Locate every blood parasite and identify its species.
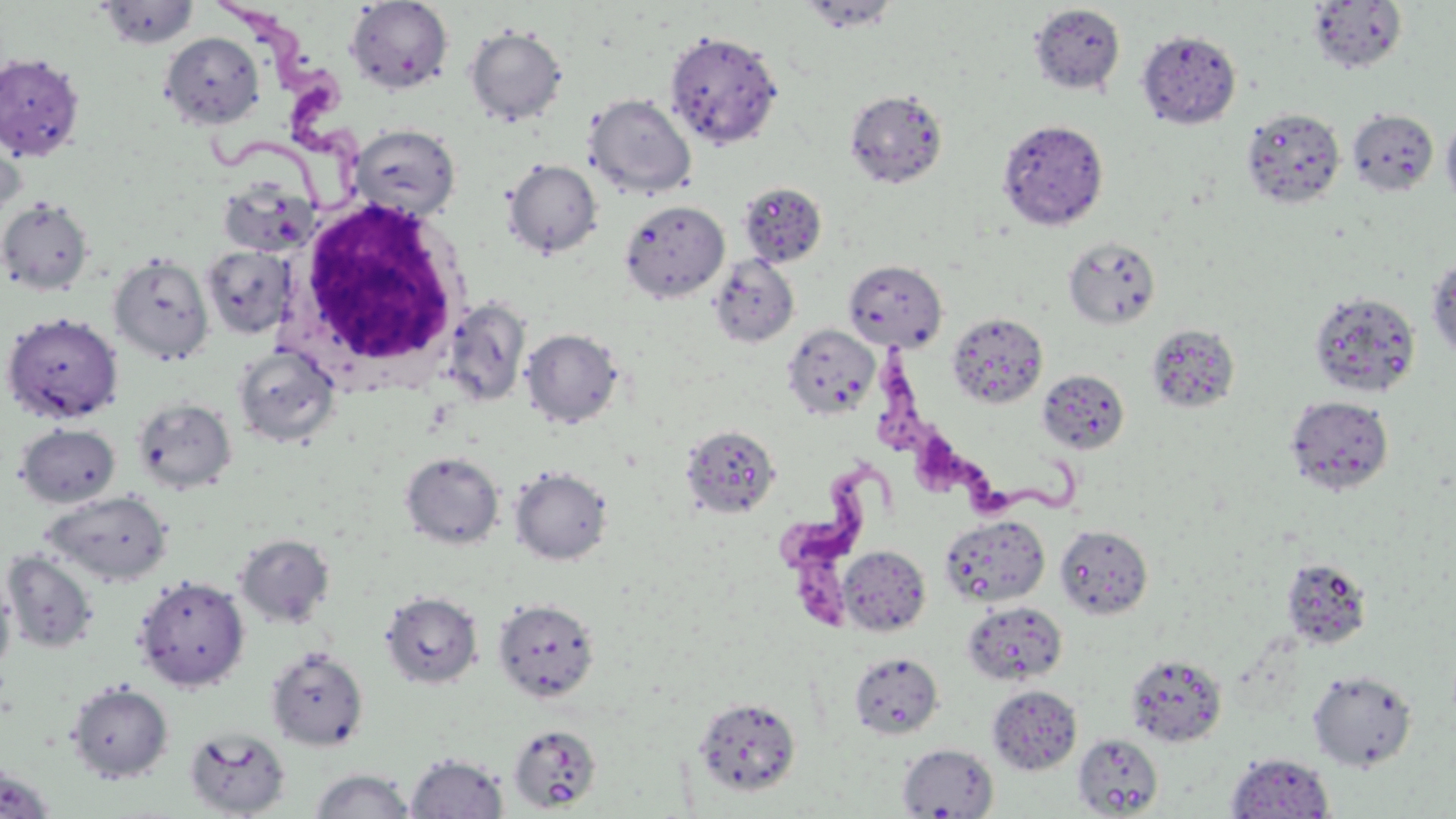
Approximate bounding boxes as (x1, y1, x2, y2) in pixels.
Trypanosoma brucei: (206, 0, 371, 211), (871, 340, 1087, 525), (775, 456, 898, 632).
No Plasmodium falciparum, Plasmodium ovale, Plasmodium malariae, Plasmodium vivax, or Babesia divergens observed.

White blood cell locations: (296, 196, 470, 373). Uninfected red blood cell locations: (797, 0, 901, 33), (96, 1, 200, 49), (345, 1, 454, 94), (1307, 1, 1407, 74), (1029, 3, 1126, 95), (464, 25, 568, 126), (1137, 29, 1241, 129), (664, 30, 783, 148), (160, 32, 264, 128), (0, 52, 86, 161), (844, 89, 949, 188), (585, 94, 697, 198), (1241, 107, 1346, 209), (1348, 109, 1439, 196), (1441, 114, 1456, 210), (997, 119, 1109, 230), (0, 121, 26, 222), (350, 124, 462, 221), (502, 159, 603, 258), (216, 175, 316, 258), (737, 182, 827, 267), (0, 197, 94, 296), (619, 199, 730, 303), (1063, 237, 1161, 328), (201, 245, 295, 340), (108, 253, 213, 365), (708, 254, 799, 348), (1426, 254, 1456, 363), (843, 259, 947, 351), (1309, 291, 1421, 398), (442, 298, 530, 407), (2, 312, 123, 424), (947, 312, 1048, 409), (1145, 323, 1240, 414), (781, 324, 880, 419), (521, 328, 623, 429), (233, 345, 341, 448), (1037, 369, 1130, 454), (133, 396, 237, 493), (1285, 396, 1394, 496), (16, 422, 121, 508), (681, 425, 781, 520), (400, 452, 504, 549), (510, 466, 613, 565), (42, 490, 173, 586), (940, 514, 1050, 607), (1054, 524, 1154, 620), (236, 534, 334, 628), (837, 546, 930, 636), (2, 551, 99, 654), (1281, 558, 1372, 650), (0, 575, 17, 676), (133, 575, 250, 691), (380, 591, 483, 689), (492, 598, 600, 702), (962, 601, 1068, 686), (266, 646, 368, 751), (848, 652, 944, 739), (1125, 652, 1228, 748), (1308, 669, 1418, 771), (67, 681, 173, 782), (987, 685, 1082, 774), (693, 697, 802, 797), (507, 723, 602, 813), (184, 726, 292, 818), (1073, 733, 1164, 816), (897, 743, 999, 818), (405, 752, 509, 819), (1225, 753, 1335, 817), (0, 761, 57, 819), (308, 768, 417, 818). Slide-level diagnosis: Trypanosoma brucei. 1000x magnification. Image is 1456×819 pixels. Light microscopy. May-Grünwald-Giemsa stain. One field of a larger specimen. Thin blood smear.